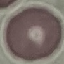
Summary:
  - Result: negative for malaria parasites
  - Capture: smartphone camera at the microscope eyepiece
  - Stain: Giemsa
  - Preparation: thin blood film
  - Image type: automatically extracted cell patch, resized to 64 × 64 pixels